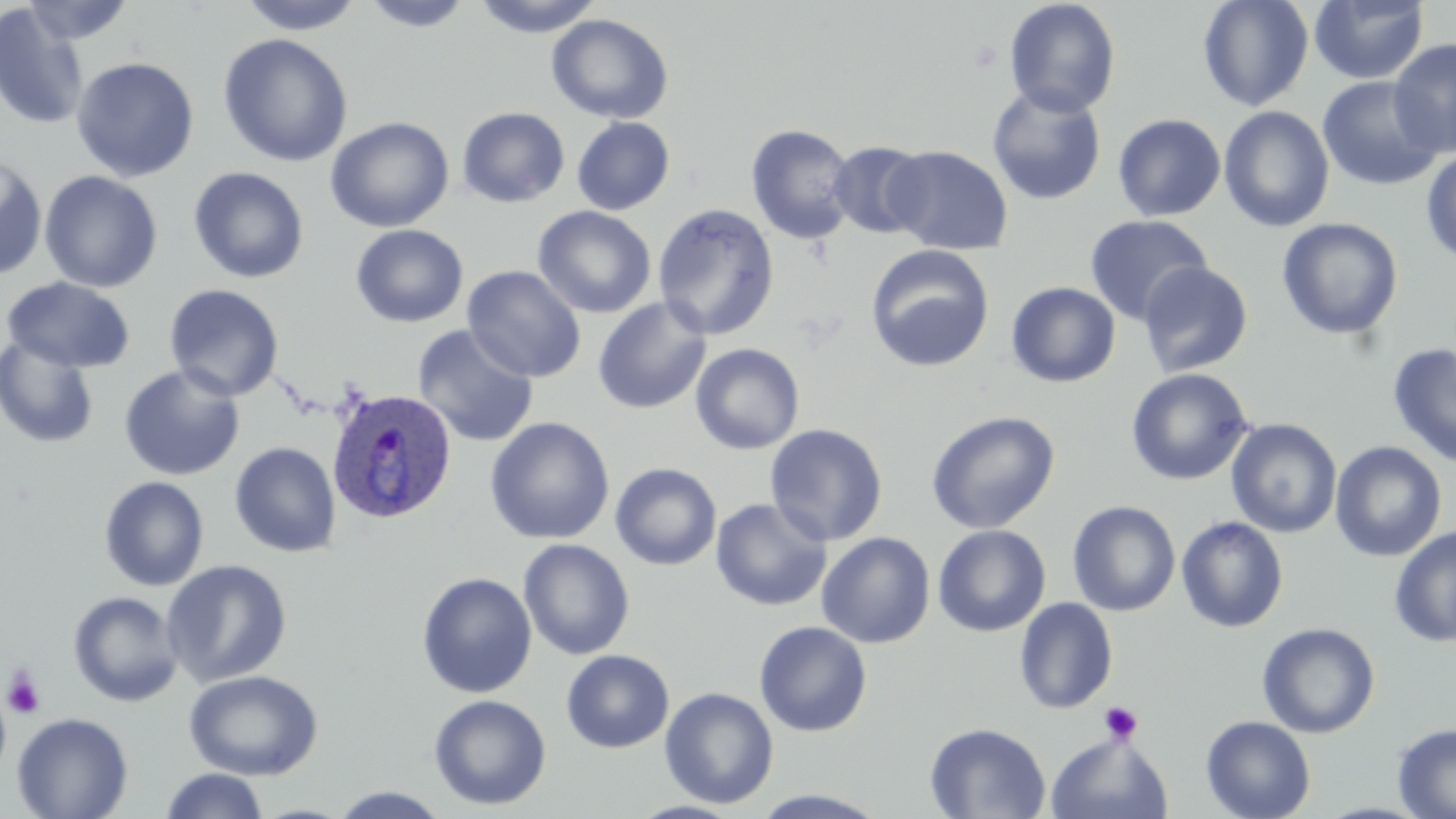
{
  "slide_level_diagnosis": "Plasmodium ovale",
  "uninfected_red_blood_cell_locations": "approximate bounding boxes as named x1/y1/x2/y2 corners in pixels: (x1=19, y1=0, x2=136, y2=46), (x1=238, y1=0, x2=365, y2=36), (x1=359, y1=0, x2=476, y2=32), (x1=472, y1=0, x2=605, y2=37), (x1=1003, y1=0, x2=1121, y2=118), (x1=1197, y1=0, x2=1315, y2=112), (x1=1309, y1=0, x2=1429, y2=84), (x1=0, y1=5, x2=90, y2=130), (x1=546, y1=14, x2=673, y2=124), (x1=217, y1=33, x2=353, y2=167), (x1=1389, y1=38, x2=1456, y2=157), (x1=70, y1=57, x2=199, y2=182), (x1=1318, y1=76, x2=1444, y2=192), (x1=986, y1=86, x2=1107, y2=206), (x1=1218, y1=106, x2=1335, y2=232), (x1=456, y1=107, x2=570, y2=208), (x1=1112, y1=114, x2=1226, y2=221), (x1=325, y1=116, x2=454, y2=233), (x1=571, y1=116, x2=675, y2=215), (x1=746, y1=123, x2=857, y2=246), (x1=828, y1=140, x2=932, y2=239), (x1=884, y1=145, x2=1013, y2=255), (x1=1421, y1=149, x2=1456, y2=266), (x1=0, y1=155, x2=48, y2=282), (x1=188, y1=167, x2=309, y2=284), (x1=39, y1=171, x2=163, y2=292), (x1=652, y1=204, x2=779, y2=340), (x1=533, y1=206, x2=657, y2=318), (x1=1084, y1=214, x2=1214, y2=326), (x1=1276, y1=218, x2=1404, y2=340), (x1=350, y1=224, x2=468, y2=328), (x1=865, y1=244, x2=995, y2=373), (x1=1137, y1=261, x2=1253, y2=378), (x1=462, y1=265, x2=587, y2=383), (x1=2, y1=278, x2=136, y2=373), (x1=1006, y1=282, x2=1121, y2=388), (x1=163, y1=284, x2=285, y2=401), (x1=592, y1=297, x2=712, y2=414), (x1=411, y1=324, x2=540, y2=448), (x1=0, y1=334, x2=100, y2=450), (x1=690, y1=343, x2=805, y2=455), (x1=1387, y1=343, x2=1456, y2=469), (x1=118, y1=364, x2=245, y2=481), (x1=1125, y1=368, x2=1254, y2=486), (x1=925, y1=410, x2=1060, y2=535), (x1=484, y1=417, x2=614, y2=544), (x1=1226, y1=419, x2=1342, y2=538), (x1=764, y1=424, x2=888, y2=546), (x1=229, y1=441, x2=341, y2=558), (x1=1330, y1=441, x2=1447, y2=562), (x1=610, y1=462, x2=722, y2=570), (x1=98, y1=476, x2=209, y2=591), (x1=710, y1=498, x2=832, y2=611), (x1=1067, y1=500, x2=1181, y2=616), (x1=1176, y1=516, x2=1289, y2=633), (x1=933, y1=525, x2=1051, y2=637), (x1=1389, y1=525, x2=1456, y2=648), (x1=816, y1=532, x2=935, y2=648), (x1=518, y1=538, x2=635, y2=660), (x1=161, y1=559, x2=292, y2=687), (x1=417, y1=572, x2=537, y2=698), (x1=67, y1=591, x2=184, y2=707), (x1=1014, y1=598, x2=1118, y2=714), (x1=754, y1=621, x2=872, y2=737), (x1=1256, y1=622, x2=1380, y2=738), (x1=561, y1=649, x2=674, y2=753), (x1=182, y1=670, x2=323, y2=780), (x1=0, y1=685, x2=11, y2=784), (x1=660, y1=687, x2=779, y2=809), (x1=429, y1=693, x2=551, y2=810), (x1=12, y1=712, x2=133, y2=819), (x1=1201, y1=716, x2=1316, y2=819), (x1=924, y1=722, x2=1051, y2=818), (x1=1392, y1=723, x2=1456, y2=818), (x1=1046, y1=732, x2=1174, y2=818), (x1=158, y1=768, x2=269, y2=819), (x1=327, y1=787, x2=449, y2=818), (x1=748, y1=789, x2=890, y2=818)",
  "platelet_locations": "approximate bounding boxes as named x1/y1/x2/y2 corners in pixels: (x1=2, y1=668, x2=45, y2=720), (x1=1099, y1=701, x2=1143, y2=744)",
  "preparation": "thin blood smear",
  "image_size": "1456×819 pixels",
  "field_of_view": "one of a larger specimen",
  "magnification": "1000x",
  "modality": "optical microscopy",
  "stain": "May-Grünwald-Giemsa",
  "plasmodium_ovale_infected_red_blood_cell_locations": "approximate bounding boxes as named x1/y1/x2/y2 corners in pixels: (x1=326, y1=387, x2=457, y2=524)"
}